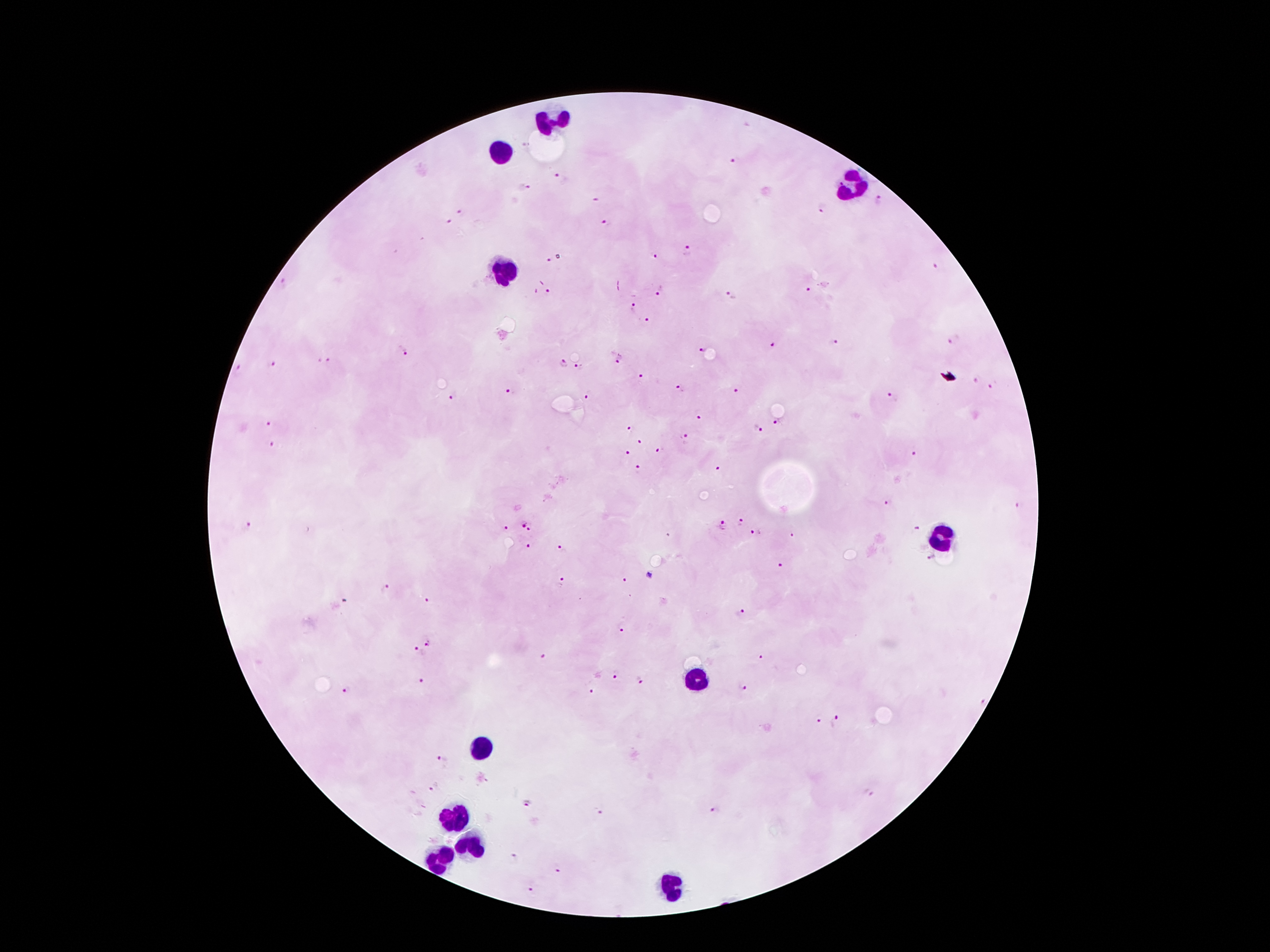

coordinate format = approximate object centers, in pixels from the top-left corner
leukocyte locations = (x=547, y=124), (x=505, y=151), (x=853, y=185), (x=503, y=277), (x=938, y=538), (x=694, y=682), (x=484, y=746), (x=453, y=818), (x=471, y=845), (x=439, y=860), (x=671, y=887)
Plasmodium parasite locations = (x=736, y=162), (x=557, y=175), (x=523, y=188), (x=878, y=200), (x=822, y=208), (x=459, y=213), (x=449, y=221), (x=606, y=225), (x=688, y=250), (x=655, y=255), (x=549, y=259), (x=937, y=266), (x=809, y=291), (x=548, y=292), (x=660, y=293), (x=733, y=296), (x=632, y=306), (x=647, y=320), (x=955, y=340), (x=834, y=341), (x=773, y=346), (x=407, y=349), (x=701, y=351), (x=618, y=359), (x=320, y=360), (x=327, y=360), (x=564, y=364), (x=275, y=365), (x=239, y=367), (x=578, y=369), (x=645, y=378), (x=976, y=380), (x=994, y=386), (x=681, y=388), (x=512, y=391), (x=733, y=391), (x=587, y=396), (x=455, y=397), (x=892, y=397), (x=697, y=416), (x=776, y=421), (x=270, y=424), (x=758, y=428), (x=630, y=430), (x=684, y=435), (x=641, y=442), (x=273, y=444), (x=660, y=450), (x=628, y=452), (x=916, y=452), (x=637, y=468), (x=716, y=469), (x=884, y=503), (x=1018, y=505), (x=741, y=523), (x=522, y=524), (x=723, y=525), (x=246, y=527), (x=916, y=527), (x=506, y=529), (x=532, y=529), (x=755, y=533), (x=792, y=534), (x=529, y=545), (x=561, y=546), (x=930, y=557), (x=779, y=566), (x=649, y=576), (x=623, y=581), (x=562, y=583), (x=386, y=588), (x=426, y=600), (x=344, y=601), (x=741, y=612), (x=621, y=628), (x=429, y=645), (x=416, y=650), (x=544, y=657), (x=762, y=657), (x=615, y=675), (x=420, y=681), (x=639, y=681), (x=741, y=687), (x=344, y=689), (x=590, y=690), (x=980, y=701), (x=817, y=720), (x=835, y=723), (x=440, y=759), (x=434, y=786), (x=868, y=794), (x=527, y=803), (x=715, y=809), (x=597, y=814), (x=514, y=855), (x=557, y=868), (x=532, y=889)
field of view = one from this slide
stain = Giemsa
patient malaria status = infected with Plasmodium falciparum
preparation = thick blood smear
image size = 1270×952 pixels
magnification = 100x
capture = smartphone camera through the microscope eyepiece